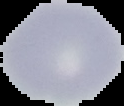
preparation = thin blood film
image size = 124×106 pixels
malaria status = uninfected
image type = segmented cell region with the area outside set to black